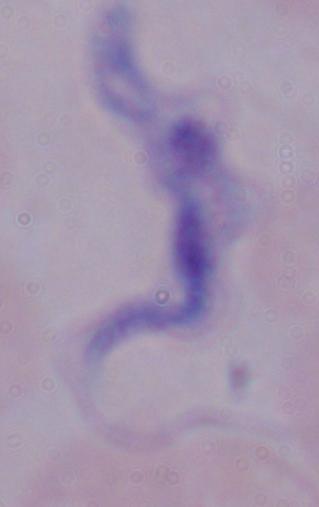

Photomicrograph. 1000x magnification. A trypanosome is shown.